Give the extent of all Trypanosoma brucei.
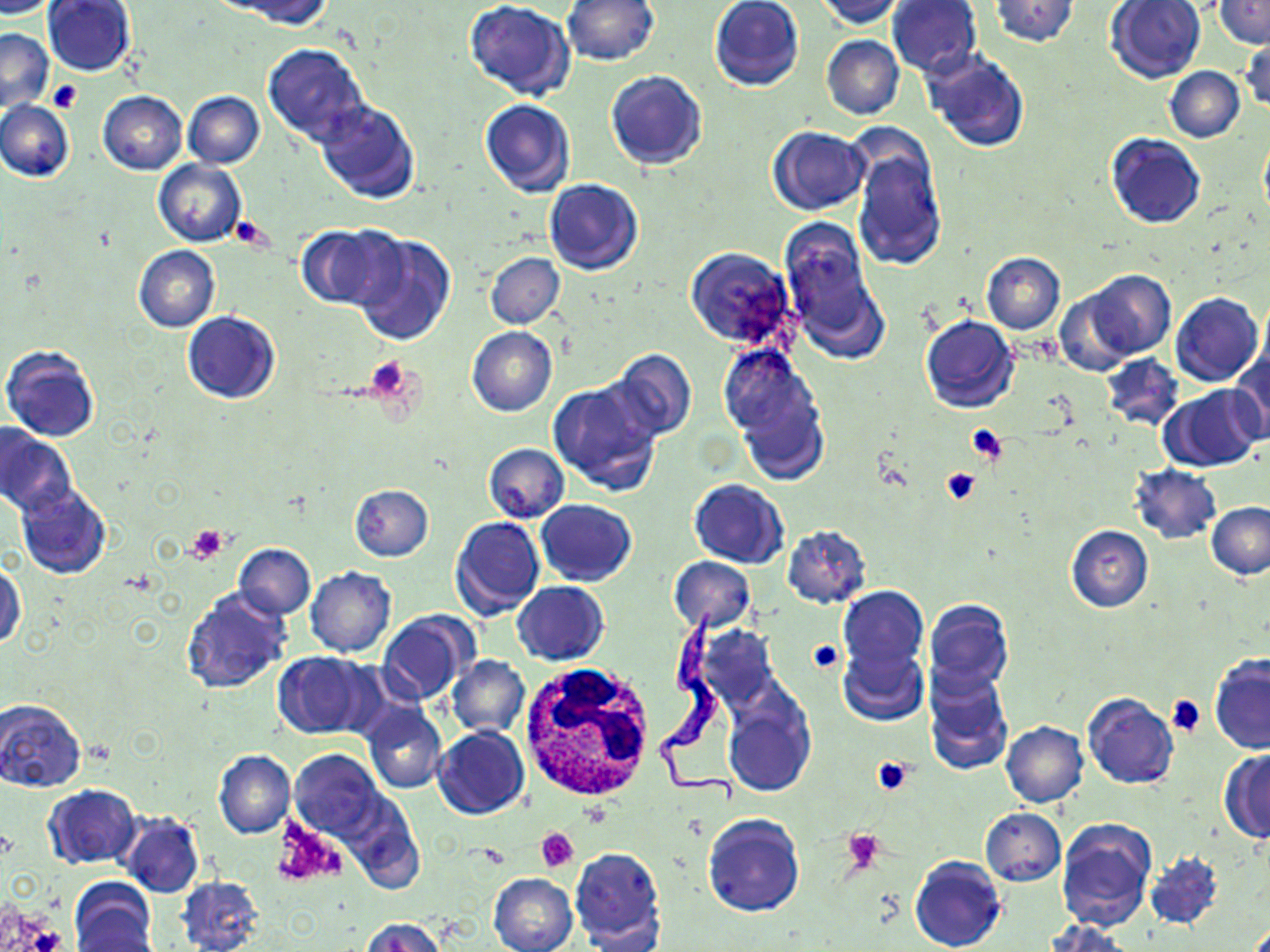

Approximate bounding boxes as (x1, y1, x2, y2) in pixels.
Trypanosoma brucei: (659, 607, 739, 803).

Platelet locations: (48, 80, 83, 115), (231, 218, 271, 249), (364, 358, 417, 405), (966, 425, 1008, 465), (940, 467, 981, 506), (185, 525, 227, 563), (807, 638, 842, 673), (1165, 694, 1206, 737), (873, 755, 917, 795), (273, 820, 345, 888), (842, 828, 884, 870), (538, 829, 578, 872). White blood cell locations: (522, 663, 656, 806). Uninfected red blood cell locations: (0, 0, 59, 19), (562, 0, 659, 66), (709, 0, 804, 92), (815, 0, 905, 28), (887, 0, 983, 76), (989, 0, 1080, 48), (1215, 0, 1270, 48), (42, 1, 136, 77), (231, 1, 339, 29), (1105, 1, 1208, 84), (464, 2, 574, 101), (0, 28, 55, 112), (822, 34, 904, 120), (1241, 35, 1269, 116), (263, 43, 369, 145), (922, 50, 1030, 154), (1164, 67, 1244, 142), (605, 70, 707, 170), (98, 91, 187, 174), (184, 91, 264, 168), (0, 99, 73, 183), (315, 99, 421, 205), (479, 99, 576, 197), (767, 126, 868, 215), (1258, 128, 1270, 225), (1106, 133, 1206, 228), (849, 140, 948, 271), (153, 160, 246, 247), (545, 179, 643, 275), (777, 217, 883, 354), (298, 224, 400, 310), (351, 231, 457, 347), (134, 245, 220, 332), (685, 246, 795, 347), (486, 252, 564, 329), (981, 252, 1065, 334), (1080, 271, 1176, 360), (1054, 286, 1140, 375), (1171, 292, 1263, 387), (1256, 292, 1270, 388), (182, 311, 280, 403), (920, 315, 1019, 413), (467, 326, 557, 416), (717, 340, 829, 474), (1, 344, 100, 444), (604, 350, 696, 444), (1228, 350, 1270, 443), (1101, 354, 1183, 432), (549, 379, 663, 496), (1160, 384, 1267, 470), (0, 427, 76, 517), (483, 443, 569, 521), (1130, 465, 1221, 543), (689, 479, 788, 569), (349, 483, 433, 561), (16, 485, 112, 580), (536, 499, 637, 585), (1206, 502, 1270, 580), (450, 516, 545, 619), (783, 524, 872, 609), (1065, 524, 1153, 612), (235, 543, 315, 618), (668, 557, 755, 634), (1, 561, 24, 652), (305, 566, 397, 658), (513, 581, 609, 665), (180, 586, 290, 695), (837, 586, 928, 674), (923, 599, 1014, 693), (377, 612, 472, 705), (695, 623, 779, 712), (838, 644, 928, 725), (274, 652, 371, 739), (447, 655, 529, 738), (1209, 655, 1270, 754), (922, 667, 1014, 775), (723, 690, 814, 798), (1082, 692, 1179, 790), (0, 697, 87, 793), (361, 703, 447, 795), (1001, 722, 1087, 807), (433, 726, 528, 820), (214, 750, 295, 838), (289, 750, 384, 840), (1219, 751, 1270, 842), (42, 785, 139, 869), (979, 808, 1065, 886), (116, 810, 205, 898), (703, 812, 805, 917), (1055, 819, 1156, 931), (569, 846, 665, 948), (1145, 851, 1225, 931), (910, 855, 1005, 952), (489, 872, 578, 952), (177, 876, 265, 952), (70, 879, 157, 950), (361, 918, 447, 952), (1046, 920, 1129, 952), (72, 923, 162, 951). Slide-level diagnosis: Trypanosoma brucei. Single field of view. May-Grünwald-Giemsa stain. Image is 1270×952 pixels. Light microscopy. Captured at 1000x magnification. Thin blood smear.